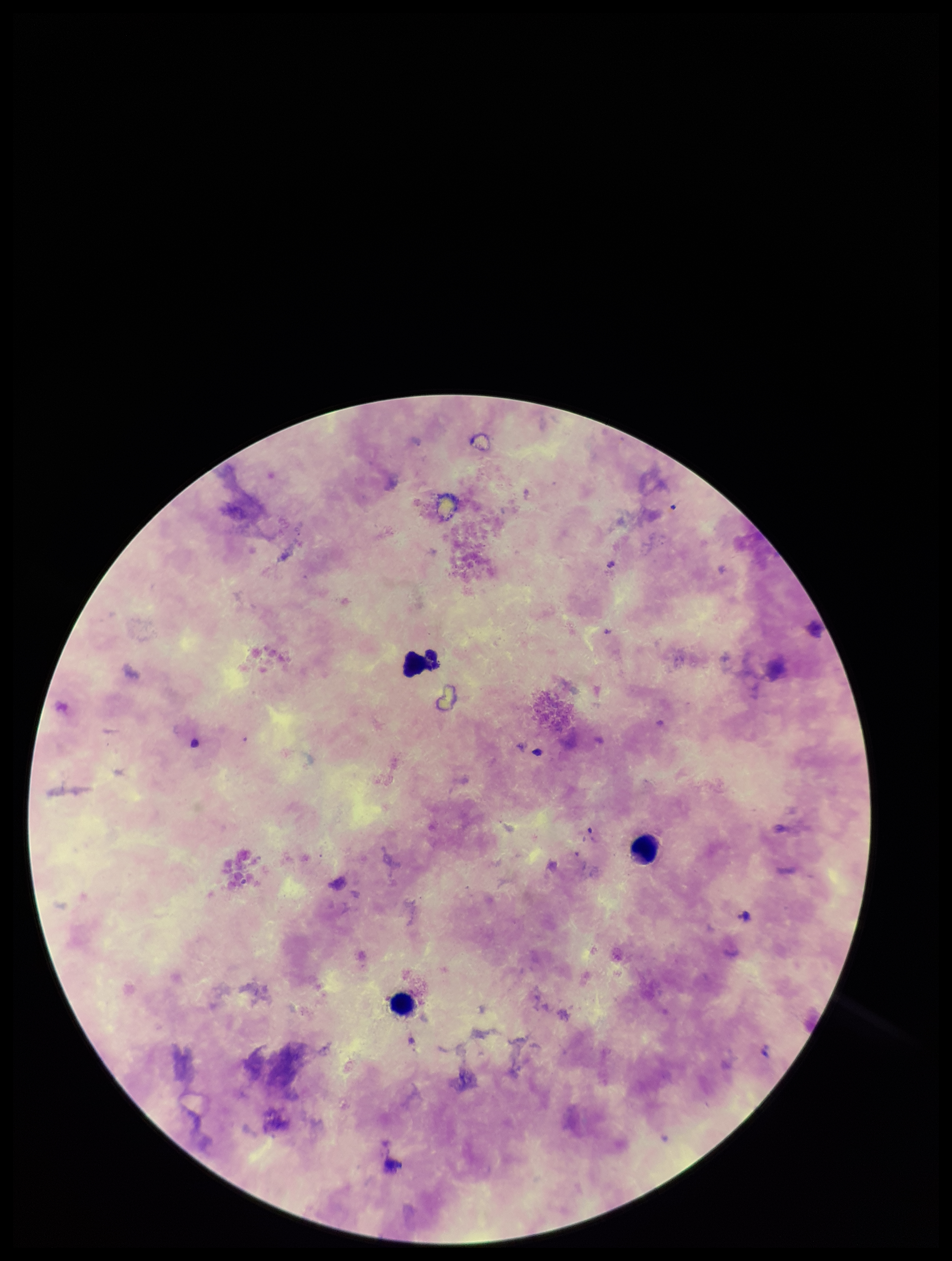

{
  "parasite_count": 0,
  "stain": "Giemsa",
  "plasmodium_parasites": "none detected",
  "field_of_view": "single",
  "image_size": "952×1261 pixels",
  "capture": "smartphone photograph through the microscope eyepiece",
  "patient_malaria_status": "negative",
  "preparation": "thick",
  "leukocyte_count": 3
}